Describe the morphology of the red blood cells.
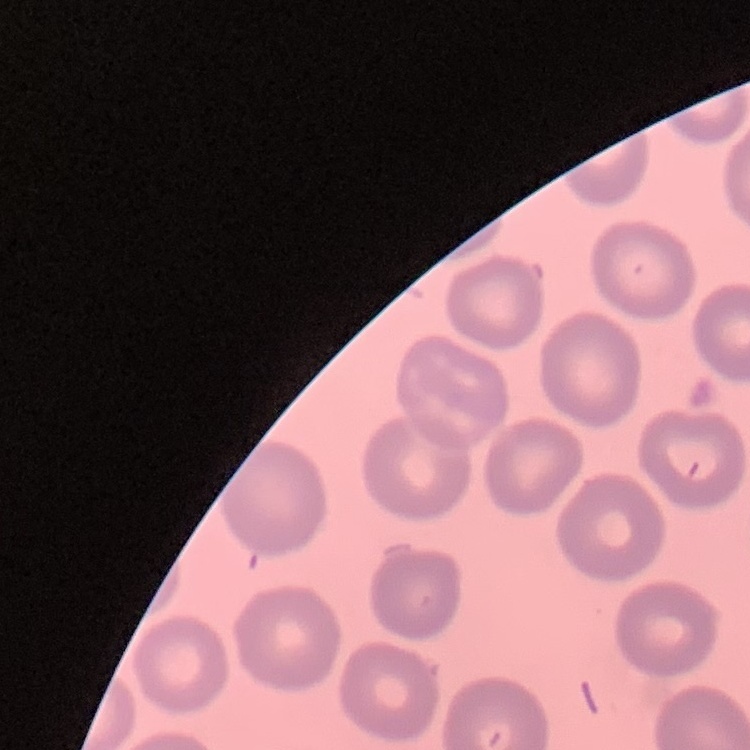

They show no rouleaux formation.

Square crop of a larger photomicrograph. Stained with either Field's or Giemsa. Thin peripheral smear.